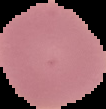
Summary:
  - Malaria status: uninfected
  - Image type: segmented cell region on a black background
  - Image size: 106×109 pixels
  - Preparation: thin blood smear